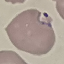
{
  "malaria_status": "parasitized",
  "preparation": "thin smear",
  "image_type": "automatically extracted cell patch, resized to 64 × 64 pixels",
  "capture": "smartphone through the microscope eyepiece",
  "stain": "Giemsa"
}